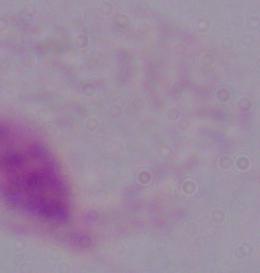
{
  "modality": "micrograph",
  "identification": "trichomonad",
  "magnification": "1000x"
}